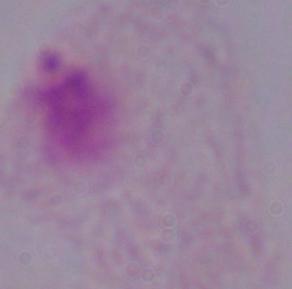
Photomicrograph. A trichomonad is seen. Captured at 1000x magnification.